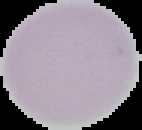
Summary:
  - Image type: segmented cell region on a black background
  - Result: no malaria parasites detected
  - Image size: 142×130 pixels
  - Preparation: thin blood smear